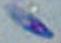

Summary:
  - Identification: Toxoplasma gondii
  - Magnification: 1000x
  - Modality: micrograph